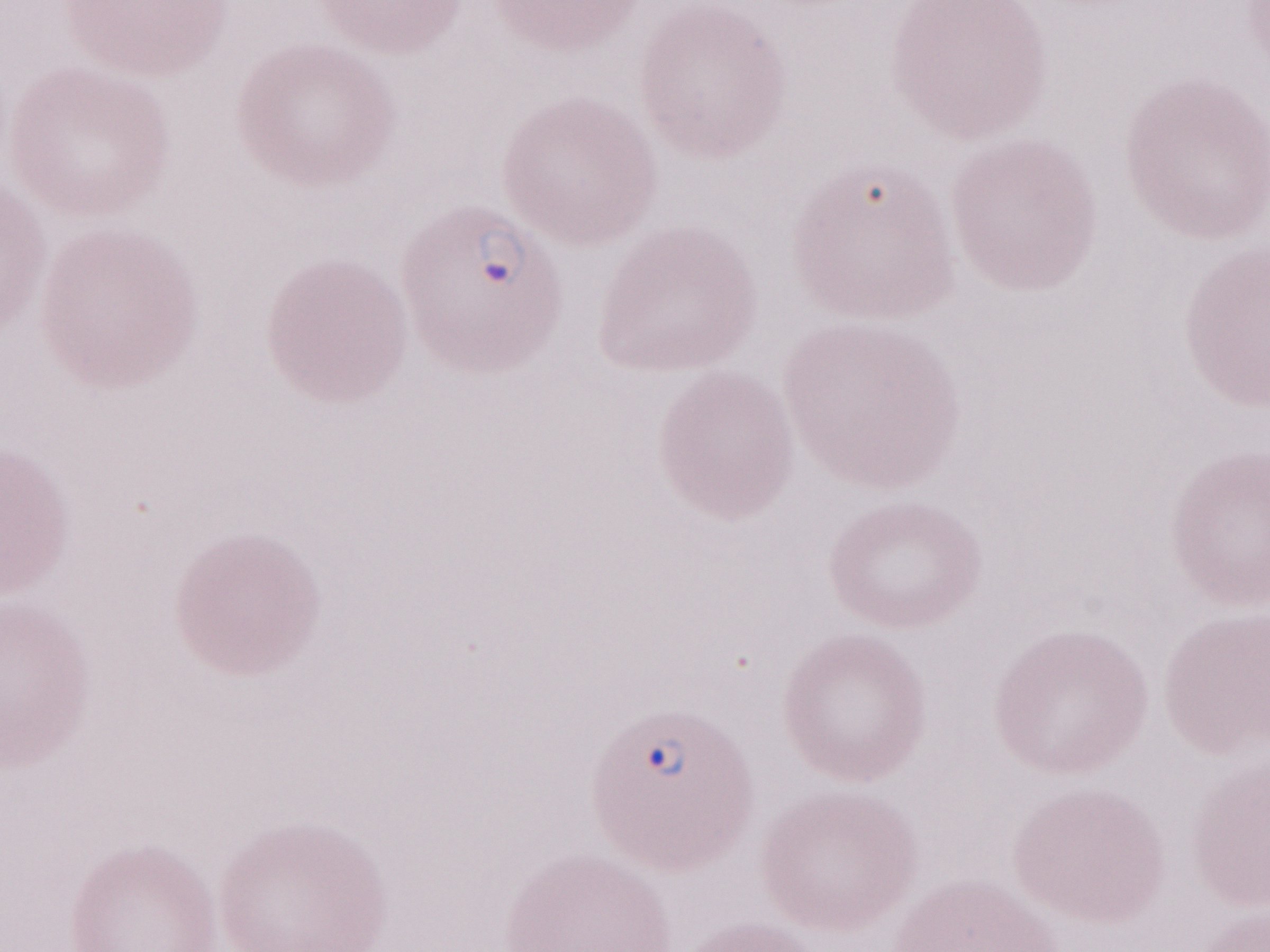

Magnification: 1,000x. Malaria diagnosis (patient-level): positive. One field of this slide. Thin blood film. Olympus BX43 microscope, Olympus DP73 camera. Image is 1270×952 pixels. May-Grünwald-Giemsa stain.